Name the parasite shown.
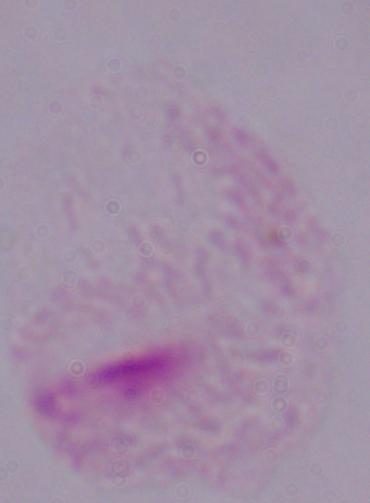
A trichomonad.

magnification = 1000x
modality = photomicrograph